Identify the parasite.
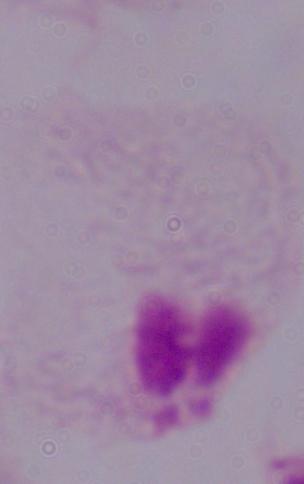

A trichomonad.

1000x magnification. Micrograph.